Assess the morphology of the red blood cells.
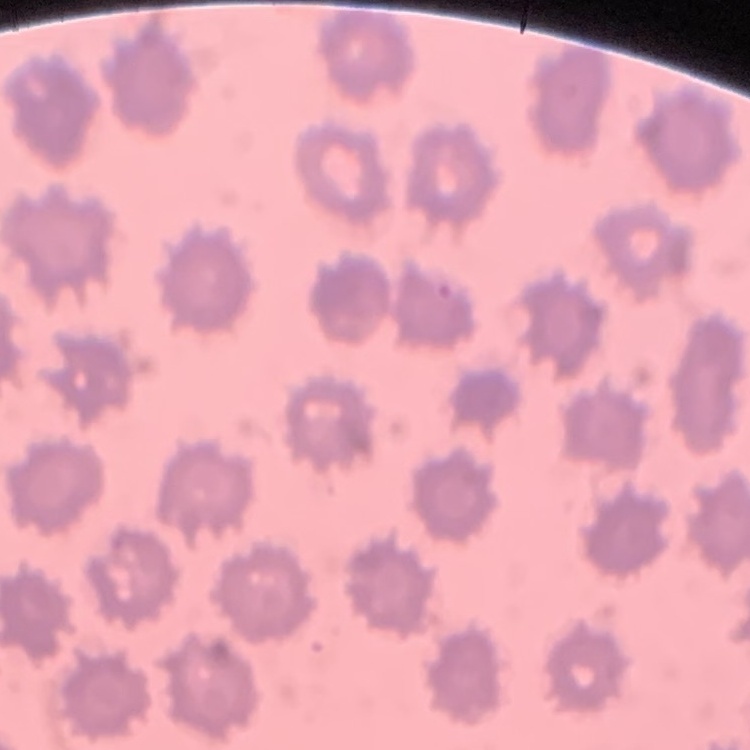

No rouleaux formation.

Summary:
  - Preparation: thin blood smear
  - Image type: one tile cut from a larger photomicrograph
  - Stain: Field's or Giemsa